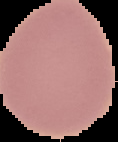

malaria status = uninfected
image type = segmented cell region on a black background
image size = 118×142 pixels
preparation = thin blood film